State which parasite is depicted.
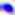
This is Toxoplasma gondii.

Micrograph. Captured at 400x magnification.